Identify the parasite.
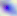

This is Toxoplasma gondii.

modality = photomicrograph
magnification = 400x